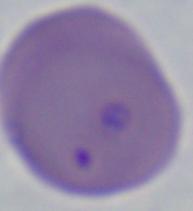 Captured at 1000x magnification. Photomicrograph. A Babesia parasite is seen.